Comment on the morphology of the red blood cells.
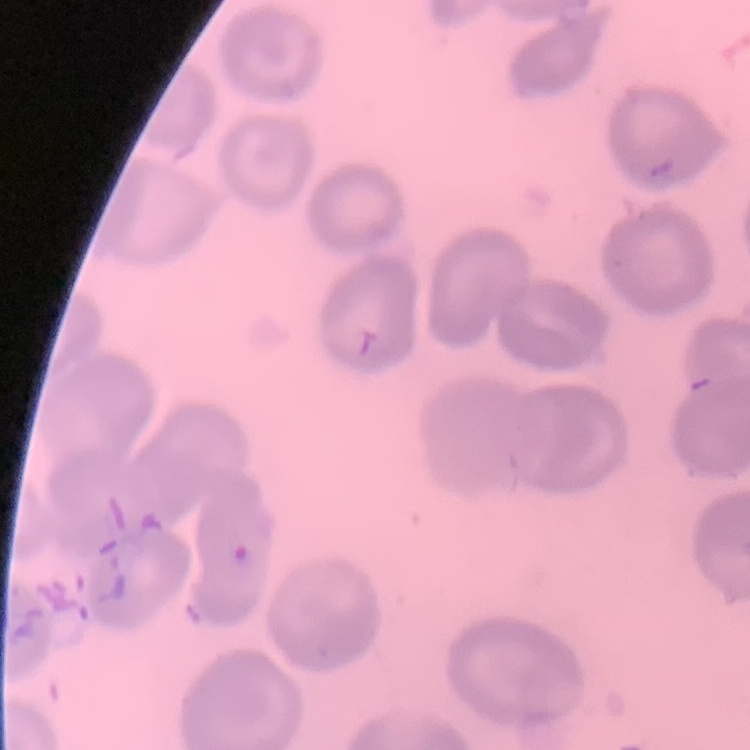
They show no rouleaux formation.

image type = square crop of a larger photomicrograph
preparation = thin blood film
stain = Field's or Giemsa